Identify the blood parasite species.
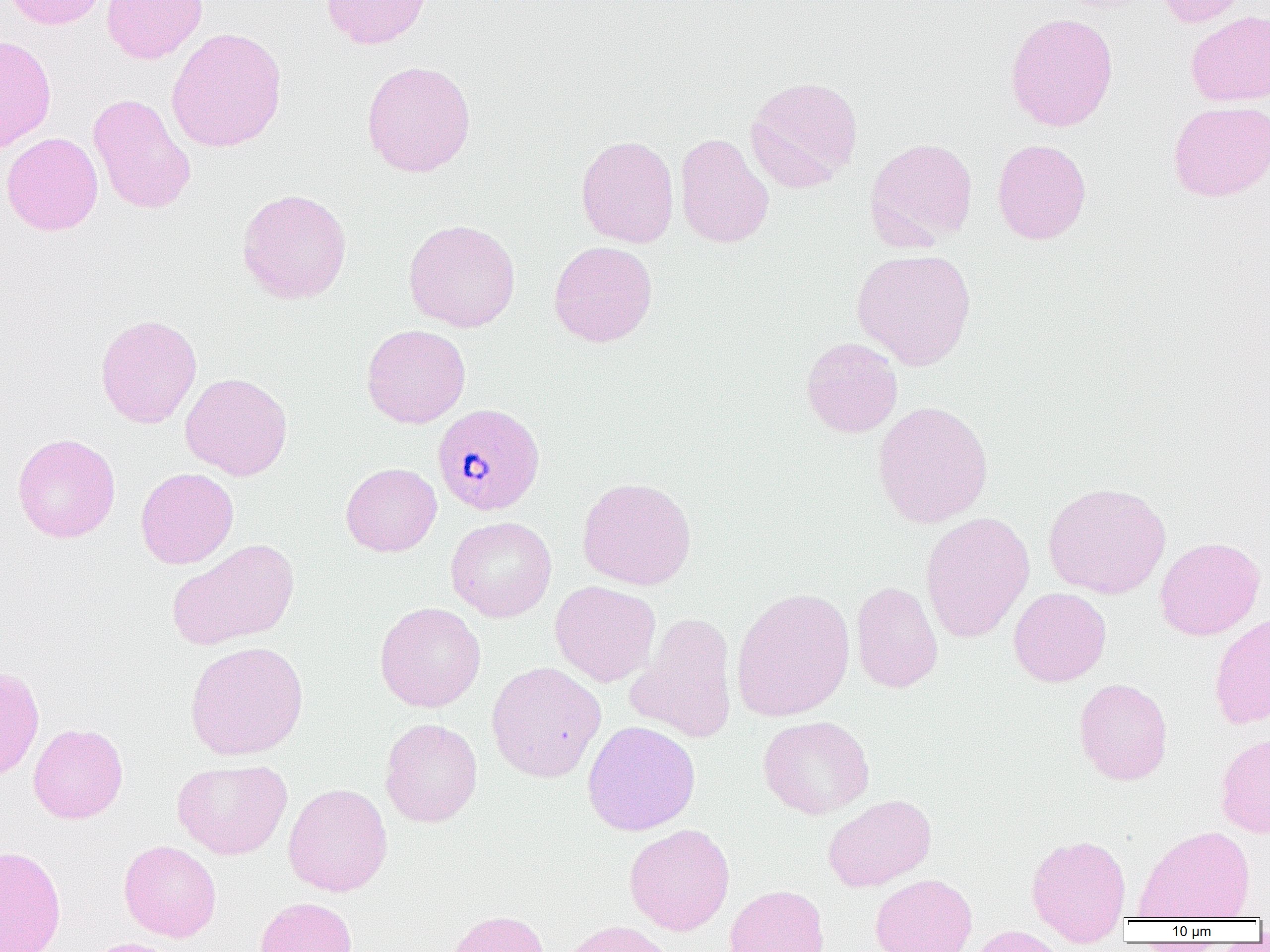
Plasmodium malariae.

Approximate bounding boxes as [x1, y1, x2, y2] in pixels. Uninfected red blood cell locations: [5, 0, 107, 29], [101, 0, 207, 64], [321, 0, 432, 49], [1155, 0, 1252, 27], [1186, 10, 1270, 106], [1005, 12, 1119, 132], [166, 27, 287, 153], [0, 34, 57, 154], [361, 60, 477, 177], [745, 76, 863, 191], [88, 94, 196, 215], [1168, 101, 1270, 202], [2, 132, 103, 235], [674, 133, 774, 249], [576, 134, 679, 248], [865, 137, 979, 250], [991, 138, 1092, 244], [236, 188, 352, 304], [403, 219, 521, 332], [548, 241, 658, 347], [852, 249, 976, 370], [95, 314, 202, 428], [361, 324, 471, 428], [801, 337, 903, 438], [181, 372, 293, 480], [872, 400, 993, 529], [12, 433, 121, 542], [341, 462, 442, 557], [135, 467, 239, 569], [577, 476, 697, 590], [1043, 481, 1171, 599], [920, 511, 1035, 643], [446, 516, 557, 622], [1155, 537, 1265, 640], [167, 538, 299, 650], [550, 581, 661, 687], [850, 581, 944, 693], [731, 587, 855, 722], [1009, 587, 1111, 687], [374, 601, 486, 712], [627, 612, 738, 743], [1209, 613, 1270, 729], [185, 641, 309, 760], [486, 661, 606, 782], [0, 666, 44, 781], [1073, 678, 1173, 785], [758, 715, 874, 819], [380, 717, 482, 827], [582, 720, 700, 836], [28, 723, 128, 823], [1215, 732, 1270, 838], [172, 759, 292, 859], [283, 783, 392, 897], [823, 794, 936, 892], [624, 823, 735, 935], [1134, 825, 1255, 921], [1025, 833, 1132, 946], [119, 840, 222, 942], [0, 845, 66, 952], [870, 873, 977, 952], [724, 884, 830, 952], [254, 896, 358, 952], [444, 909, 551, 952], [558, 920, 678, 952], [968, 925, 1068, 952], [80, 937, 183, 952]. Plasmodium malariae-infected red blood cell locations: [431, 402, 546, 517]. Light microscopy. Image is 1270×952 pixels. 1000x magnification. Thin blood film. One field of a larger specimen.